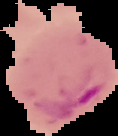
From a thin blood film. Result: Plasmodium parasites detected. The area outside the segmented cell region is set to black. Image is 118×136 pixels.